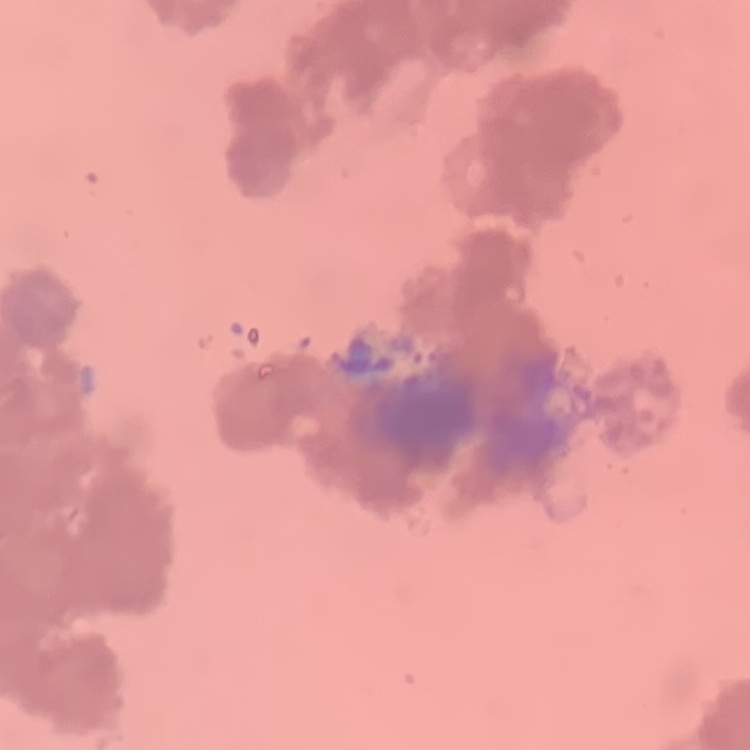
The erythrocytes exhibit rouleaux formation. Square crop of a larger photomicrograph. Stained with either Field's or Giemsa. Thin blood film.